Locate every blood parasite and identify its species.
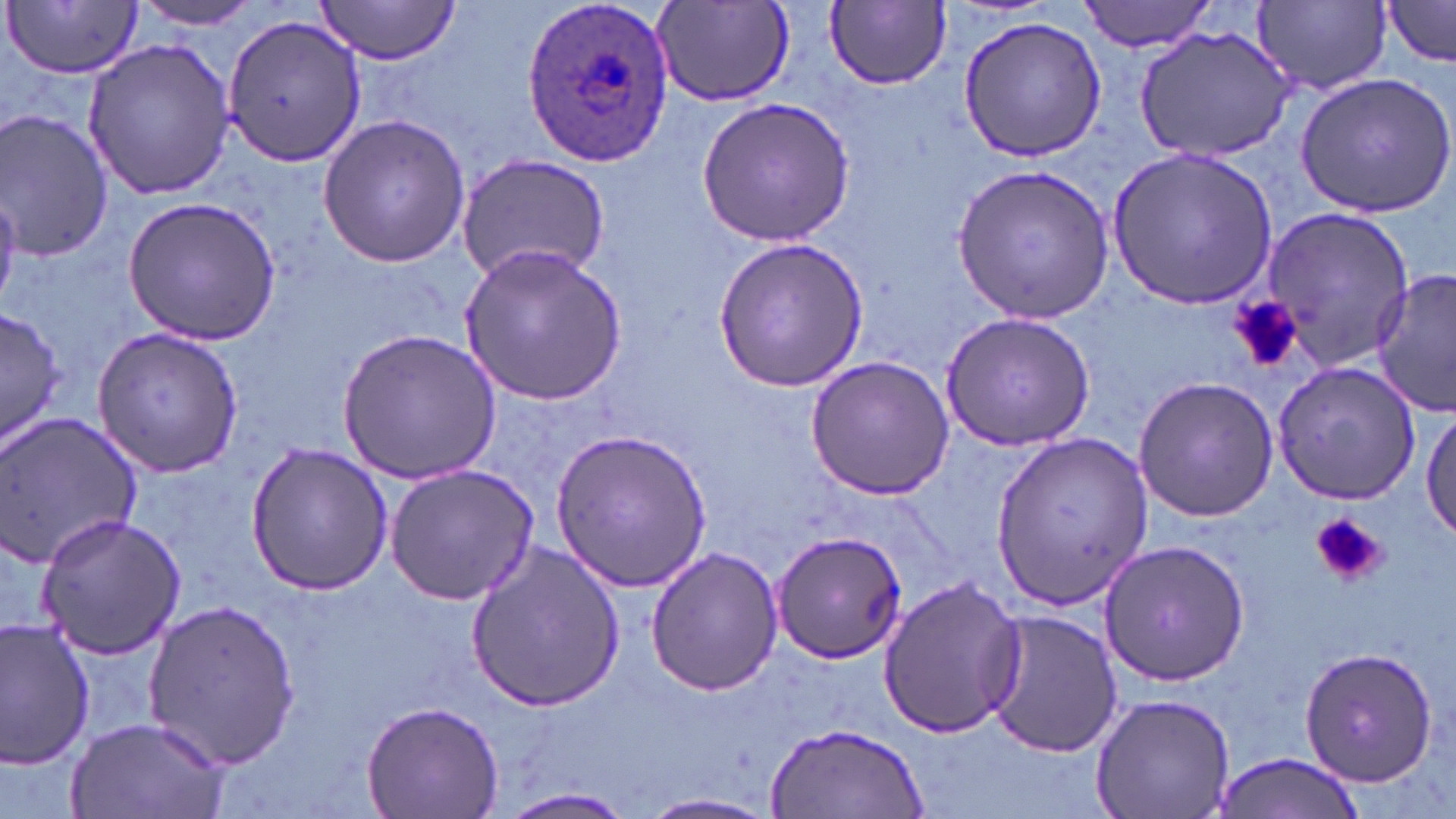

Approximate bounding boxes as (x1, y1, x2, y2) in pixels.
Plasmodium ovale-infected red blood cells: (519, 3, 673, 165).
No Plasmodium falciparum, Plasmodium malariae, Plasmodium vivax, Babesia divergens, or Trypanosoma brucei observed.

slide_level_diagnosis: Plasmodium ovale
stain: May-Grünwald-Giemsa
field_of_view: one of a larger specimen
magnification: 1000x
modality: light microscopy
image_size: 1456×819 pixels
preparation: thin blood film
platelet_locations: 'approximate bounding boxes as (x1, y1, x2, y2) in pixels: (1230, 298, 1301, 371), (1309, 513, 1387, 587)'
uninfected_red_blood_cell_locations: 'approximate bounding boxes as (x1, y1, x2, y2) in pixels: (130, 0, 270, 30), (311, 0, 463, 64), (1077, 0, 1216, 54), (1252, 0, 1390, 93), (1379, 0, 1456, 66), (649, 1, 798, 108), (826, 1, 952, 89), (6, 2, 143, 78), (221, 14, 368, 166), (958, 14, 1107, 161), (1135, 24, 1299, 164), (80, 37, 234, 201), (1293, 71, 1455, 218), (698, 96, 854, 245), (0, 111, 115, 262), (314, 112, 473, 270), (1107, 147, 1278, 311), (456, 152, 612, 285), (953, 165, 1114, 322), (121, 196, 281, 343), (1255, 205, 1411, 372), (712, 237, 869, 391), (457, 243, 632, 407), (1372, 270, 1456, 417), (0, 306, 65, 455), (940, 312, 1095, 452), (93, 326, 246, 477), (337, 328, 500, 483), (804, 358, 955, 501), (1275, 362, 1423, 504), (1133, 376, 1280, 521), (1421, 405, 1455, 546), (0, 412, 146, 569), (553, 427, 712, 590), (989, 430, 1151, 609), (242, 442, 394, 596), (384, 464, 540, 604), (36, 512, 189, 660), (771, 528, 910, 664), (1098, 538, 1251, 687), (464, 543, 626, 712), (645, 546, 785, 696), (878, 576, 1029, 741), (143, 597, 302, 773), (981, 608, 1124, 760), (0, 617, 97, 771), (1299, 644, 1439, 788), (1090, 693, 1236, 819), (359, 697, 506, 819), (64, 714, 229, 819), (765, 719, 930, 817), (1208, 752, 1368, 818), (499, 788, 639, 817), (640, 792, 779, 818)'